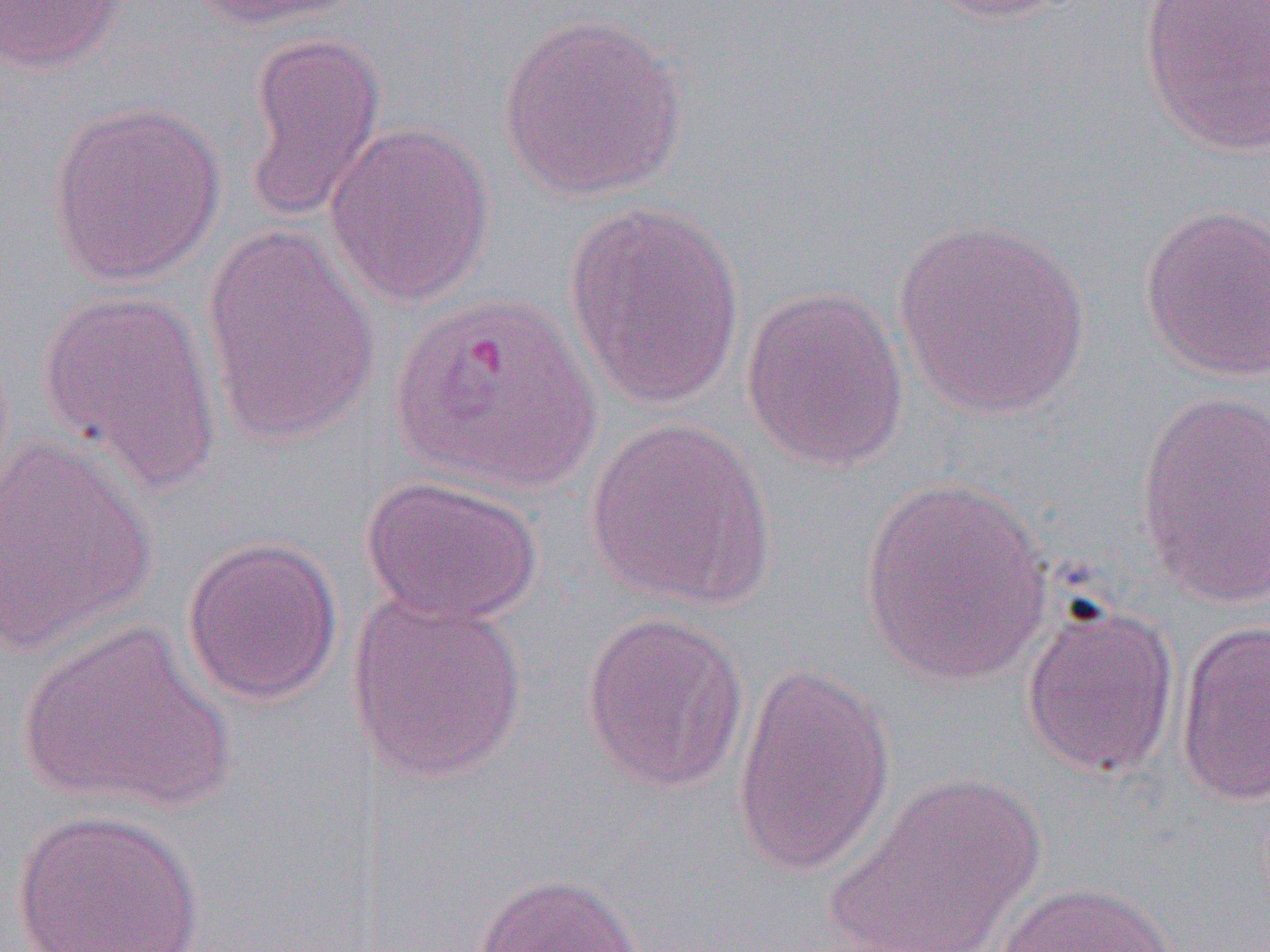

{
  "slide_level_diagnosis": "Plasmodium vivax",
  "field_of_view": "one of a larger specimen",
  "preparation": "thin blood smear",
  "modality": "optical microscopy",
  "image_size": "1270×952 pixels",
  "uninfected_red_blood_cell_locations": "approximate bounding boxes as named x1/y1/x2/y2 corners in pixels: (x1=0, y1=0, x2=125, y2=74), (x1=192, y1=0, x2=364, y2=31), (x1=917, y1=0, x2=1086, y2=25), (x1=1139, y1=0, x2=1270, y2=156), (x1=496, y1=11, x2=689, y2=202), (x1=243, y1=31, x2=386, y2=223), (x1=46, y1=100, x2=227, y2=289), (x1=324, y1=121, x2=495, y2=308), (x1=562, y1=201, x2=747, y2=411), (x1=1139, y1=202, x2=1270, y2=382), (x1=894, y1=216, x2=1092, y2=419), (x1=199, y1=222, x2=382, y2=449), (x1=740, y1=286, x2=909, y2=472), (x1=36, y1=287, x2=223, y2=493), (x1=1135, y1=388, x2=1270, y2=611), (x1=583, y1=416, x2=776, y2=611), (x1=0, y1=434, x2=158, y2=658), (x1=360, y1=475, x2=543, y2=626), (x1=858, y1=476, x2=1056, y2=688), (x1=181, y1=534, x2=343, y2=707), (x1=346, y1=590, x2=529, y2=784), (x1=1020, y1=601, x2=1180, y2=779), (x1=581, y1=612, x2=749, y2=794), (x1=17, y1=618, x2=234, y2=812), (x1=1175, y1=620, x2=1270, y2=806), (x1=730, y1=661, x2=897, y2=880), (x1=826, y1=773, x2=1049, y2=950), (x1=10, y1=808, x2=207, y2=952), (x1=472, y1=872, x2=643, y2=952), (x1=992, y1=882, x2=1182, y2=951)",
  "magnification": "1000x"
}